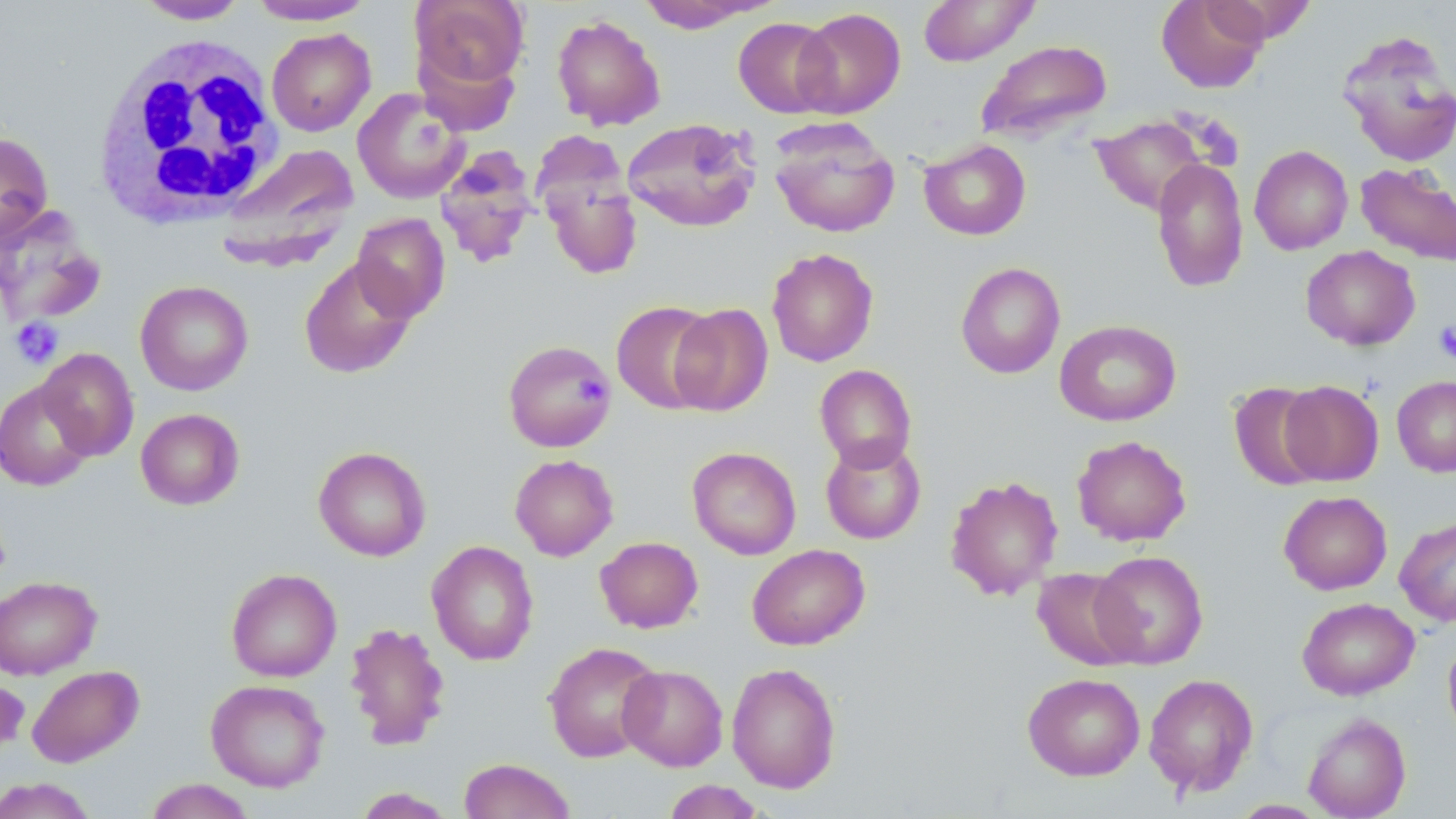
Summary:
  - Coordinate format: approximate bounding boxes as named x1/y1/x2/y2 corners in pixels
  - Uninfected red blood cell locations (subset): (x1=248, y1=0, x2=377, y2=26), (x1=410, y1=0, x2=529, y2=93), (x1=635, y1=0, x2=774, y2=32), (x1=918, y1=0, x2=1040, y2=66), (x1=1156, y1=0, x2=1269, y2=93), (x1=134, y1=1, x2=249, y2=25), (x1=794, y1=7, x2=906, y2=118), (x1=551, y1=13, x2=666, y2=131), (x1=733, y1=17, x2=838, y2=118), (x1=266, y1=28, x2=376, y2=136), (x1=1336, y1=30, x2=1456, y2=168), (x1=976, y1=39, x2=1112, y2=143), (x1=352, y1=88, x2=470, y2=203), (x1=1091, y1=116, x2=1208, y2=216), (x1=622, y1=118, x2=761, y2=233), (x1=768, y1=119, x2=900, y2=238), (x1=0, y1=132, x2=53, y2=244), (x1=918, y1=139, x2=1031, y2=241), (x1=218, y1=143, x2=359, y2=268), (x1=1249, y1=145, x2=1353, y2=255), (x1=434, y1=149, x2=538, y2=268), (x1=538, y1=155, x2=643, y2=282), (x1=1152, y1=158, x2=1249, y2=293), (x1=1355, y1=162, x2=1456, y2=266), (x1=351, y1=213, x2=451, y2=321), (x1=1301, y1=245, x2=1420, y2=351), (x1=766, y1=247, x2=879, y2=367), (x1=299, y1=257, x2=418, y2=379), (x1=955, y1=261, x2=1066, y2=379), (x1=135, y1=280, x2=254, y2=395), (x1=611, y1=300, x2=720, y2=414), (x1=668, y1=303, x2=773, y2=416), (x1=1054, y1=319, x2=1181, y2=426), (x1=502, y1=339, x2=618, y2=453), (x1=37, y1=347, x2=139, y2=460), (x1=814, y1=364, x2=917, y2=471), (x1=1392, y1=375, x2=1456, y2=477), (x1=0, y1=379, x2=97, y2=491), (x1=1278, y1=380, x2=1384, y2=486), (x1=1228, y1=382, x2=1328, y2=490), (x1=135, y1=408, x2=245, y2=509), (x1=1072, y1=435, x2=1192, y2=546), (x1=820, y1=437, x2=927, y2=544), (x1=313, y1=446, x2=431, y2=561), (x1=687, y1=446, x2=802, y2=560), (x1=509, y1=454, x2=618, y2=561), (x1=944, y1=475, x2=1063, y2=601), (x1=1278, y1=491, x2=1392, y2=595), (x1=1394, y1=516, x2=1456, y2=626), (x1=595, y1=536, x2=703, y2=633), (x1=426, y1=540, x2=539, y2=665), (x1=747, y1=543, x2=870, y2=650), (x1=1089, y1=550, x2=1209, y2=668), (x1=1032, y1=567, x2=1140, y2=670), (x1=226, y1=568, x2=342, y2=682), (x1=0, y1=575, x2=102, y2=680), (x1=1297, y1=597, x2=1419, y2=700), (x1=344, y1=621, x2=451, y2=751), (x1=1443, y1=633, x2=1456, y2=745), (x1=543, y1=642, x2=663, y2=762), (x1=726, y1=662, x2=842, y2=793), (x1=26, y1=664, x2=144, y2=767), (x1=617, y1=664, x2=728, y2=770), (x1=1022, y1=673, x2=1145, y2=780), (x1=1143, y1=673, x2=1259, y2=797), (x1=205, y1=679, x2=330, y2=792), (x1=1302, y1=712, x2=1412, y2=819), (x1=458, y1=758, x2=577, y2=819), (x1=0, y1=777, x2=98, y2=818), (x1=144, y1=779, x2=256, y2=819), (x1=662, y1=780, x2=766, y2=819), (x1=352, y1=787, x2=456, y2=818), (x1=1231, y1=800, x2=1330, y2=818)
  - Platelet locations (subset): (x1=1181, y1=111, x2=1243, y2=167), (x1=10, y1=318, x2=64, y2=369), (x1=1434, y1=320, x2=1456, y2=364), (x1=575, y1=375, x2=607, y2=404)
  - White blood cell locations: (x1=90, y1=34, x2=286, y2=227)
  - Slide-level diagnosis: negative for blood parasites
  - Modality: light microscopy
  - Stain: May-Grünwald-Giemsa
  - Field of view: single
  - Image size: 1456×819 pixels
  - Magnification: 1000x
  - Preparation: thin blood film